State the blood parasite species.
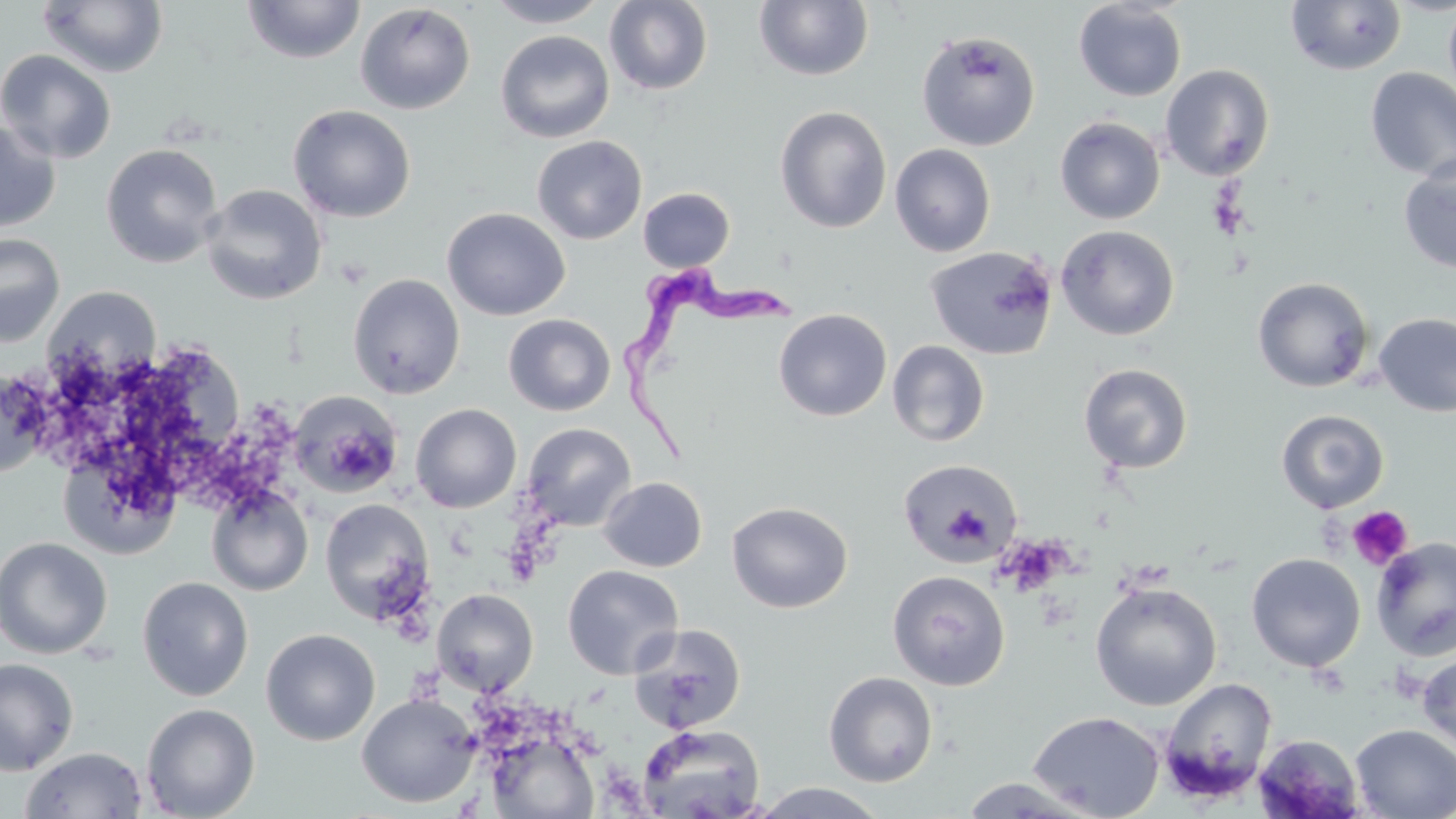
Trypanosoma brucei.

Approximate bounding boxes as [x1, y1, x2, y2] in pixels. Uninfected red blood cell locations: [242, 0, 365, 65], [484, 0, 611, 28], [604, 0, 713, 95], [753, 0, 875, 82], [1073, 0, 1188, 102], [1285, 0, 1407, 75], [1443, 0, 1456, 103], [37, 1, 168, 78], [354, 3, 476, 115], [495, 30, 615, 144], [916, 31, 1040, 151], [0, 49, 117, 165], [1159, 64, 1275, 181], [1364, 67, 1456, 182], [287, 104, 416, 223], [774, 105, 892, 234], [1054, 116, 1165, 224], [0, 119, 61, 233], [532, 135, 647, 245], [100, 143, 224, 269], [890, 143, 996, 257], [1398, 155, 1456, 275], [201, 184, 327, 305], [637, 187, 735, 272], [442, 207, 571, 321], [1055, 225, 1179, 340], [0, 233, 65, 347], [925, 246, 1058, 360], [347, 273, 465, 399], [1252, 277, 1375, 392], [43, 286, 161, 384], [773, 309, 892, 422], [1373, 312, 1456, 417], [503, 313, 616, 416], [887, 340, 990, 447], [1079, 363, 1194, 474], [0, 370, 54, 479], [289, 390, 405, 498], [411, 403, 522, 513], [1276, 409, 1389, 513], [522, 423, 636, 532], [897, 458, 1024, 567], [598, 476, 707, 572], [206, 485, 313, 597], [319, 498, 435, 624], [727, 501, 853, 613], [0, 536, 113, 659], [1371, 537, 1456, 660], [1246, 553, 1366, 672], [562, 565, 684, 680], [887, 570, 1011, 690], [137, 576, 254, 701], [1089, 581, 1222, 711], [432, 589, 539, 697], [629, 623, 746, 734], [261, 628, 380, 745], [1417, 652, 1456, 760], [0, 657, 79, 775], [823, 671, 938, 787], [1159, 677, 1277, 802], [356, 692, 481, 808], [141, 703, 260, 819], [1028, 710, 1165, 819], [637, 723, 765, 819], [1350, 724, 1456, 818], [485, 731, 601, 818], [1254, 733, 1366, 818], [19, 746, 148, 818], [957, 777, 1099, 818], [750, 782, 891, 818]. Trypanosoma brucei locations: [613, 270, 800, 467]. Platelet locations: [1347, 505, 1413, 570]. Thin blood smear. May-Grünwald-Giemsa-stained preparation. Image is 1456×819 pixels. One field of a larger specimen. Captured at 1000x magnification. Optical microscopy.